Describe the morphology of the red blood cells.
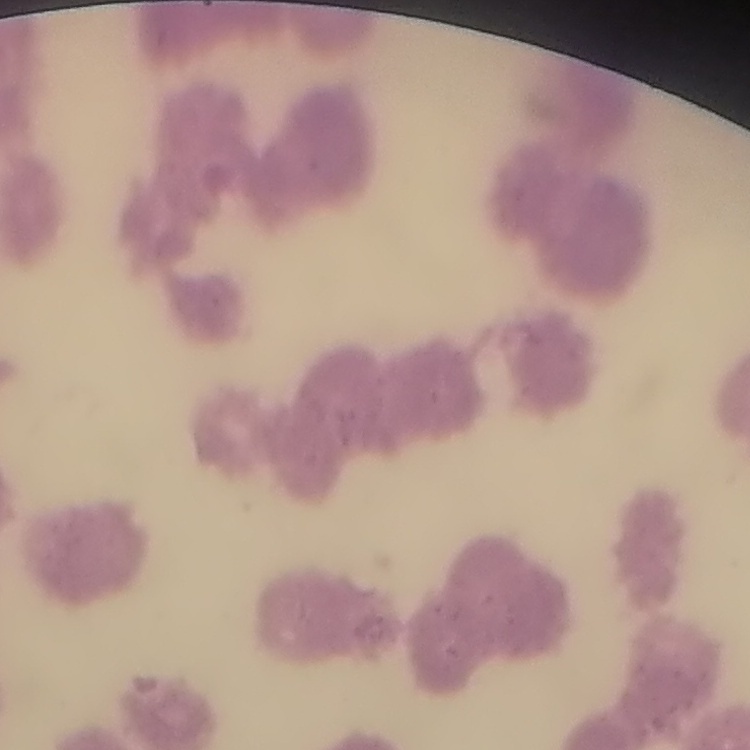
They show rouleaux formation.

Square crop of a larger photomicrograph. Thin blood film. Field's or Giemsa stain.